Name the parasite shown.
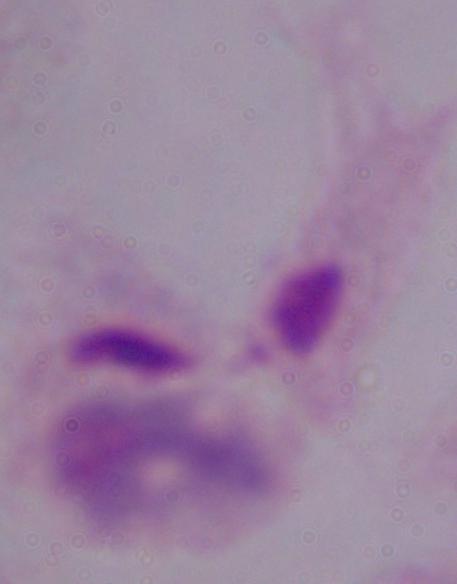
A trichomonad.

1000x magnification. Photomicrograph.